State which cell type is depicted.
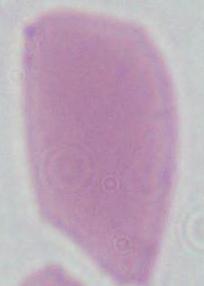
This is an erythrocyte.

Summary:
  - Magnification: 1000x
  - Modality: photomicrograph